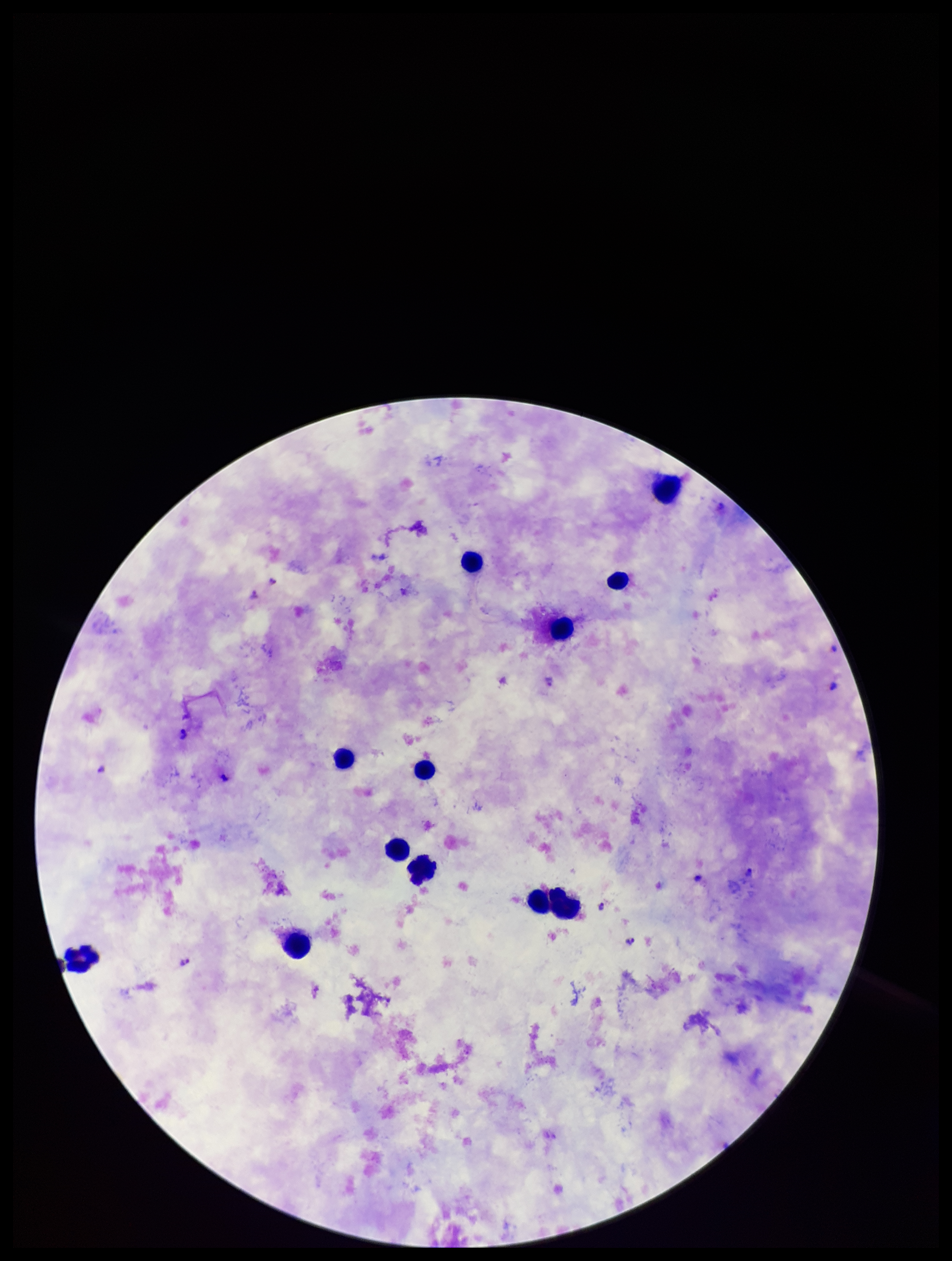

Smartphone photograph taken through the eyepiece of a microscope. Patient malaria status: positive. Leukocyte count: 12. Parasite count: 8. Plasmodium parasites: detected. One field from this slide. Giemsa stain. Species reported for this patient: Plasmodium falciparum. Image is 952×1261 pixels. Preparation: thick blood smear.